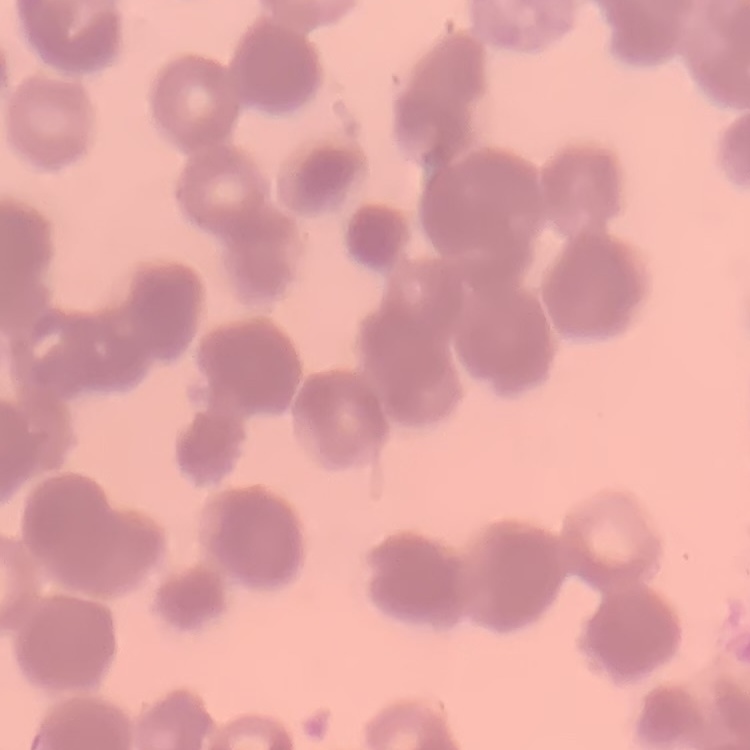

{
  "erythrocyte_morphology": "rouleaux formation",
  "preparation": "thin blood smear",
  "image_type": "square crop of a larger photomicrograph",
  "stain": "Field's or Giemsa"
}